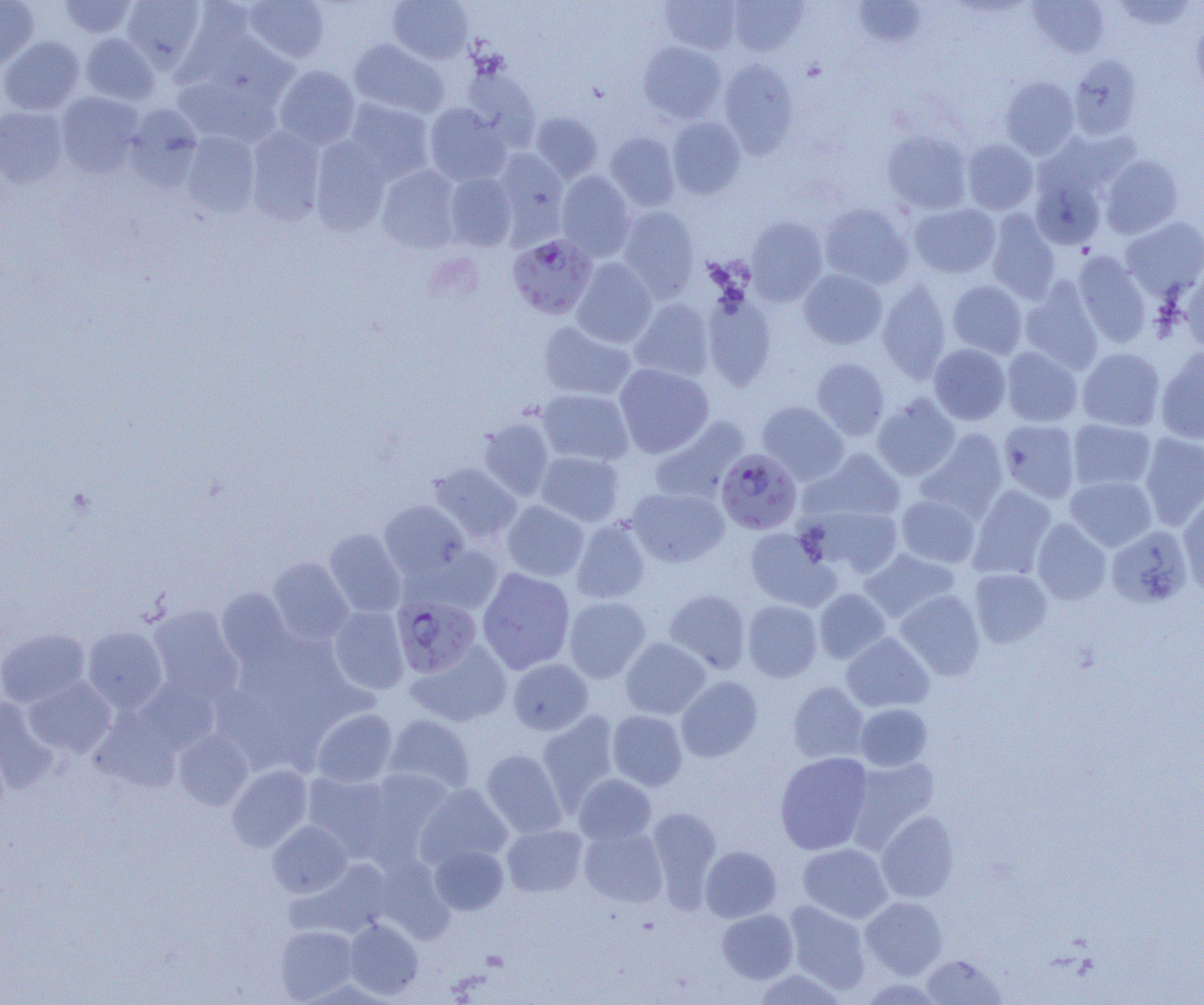 Approximate bounding boxes as (x1, y1, x2, y2) in pixels. Plasmodium falciparum-infected red blood cell locations: (507, 233, 597, 319), (716, 448, 801, 534), (392, 595, 482, 678). Uninfected red blood cell locations: (0, 0, 39, 70), (57, 0, 138, 39), (121, 0, 206, 71), (243, 0, 330, 63), (387, 0, 474, 64), (660, 0, 741, 54), (729, 0, 807, 56), (852, 0, 926, 48), (1027, 1, 1110, 59), (1109, 1, 1199, 31), (161, 3, 254, 89), (1192, 16, 1204, 100), (80, 33, 160, 105), (0, 36, 85, 115), (349, 38, 449, 118), (639, 41, 725, 123), (1069, 55, 1143, 140), (719, 59, 798, 156), (273, 65, 361, 149), (462, 67, 540, 148), (1000, 76, 1079, 158), (171, 84, 285, 146), (55, 92, 144, 176), (343, 98, 435, 184), (424, 103, 512, 186), (124, 104, 204, 189), (0, 106, 68, 188), (530, 111, 603, 183), (667, 117, 746, 198), (246, 127, 326, 224), (882, 130, 973, 215), (180, 132, 260, 217), (604, 132, 681, 211), (309, 137, 391, 235), (962, 139, 1038, 215), (492, 149, 569, 239), (1100, 154, 1184, 238), (377, 165, 463, 252), (556, 171, 635, 261), (444, 172, 517, 251), (1030, 173, 1106, 251), (819, 203, 914, 289), (908, 203, 1000, 278), (617, 206, 700, 301), (986, 210, 1061, 303), (745, 216, 828, 306), (1120, 216, 1204, 299), (1073, 252, 1152, 346), (571, 258, 658, 348), (1180, 268, 1204, 352), (798, 269, 887, 349), (877, 279, 951, 381), (947, 280, 1027, 358), (1020, 280, 1104, 373), (702, 294, 776, 390), (629, 298, 714, 382), (538, 321, 636, 401), (929, 344, 1011, 425), (1001, 346, 1083, 427), (1156, 346, 1204, 445), (1077, 347, 1165, 432), (811, 358, 890, 440), (614, 363, 713, 457), (537, 389, 634, 466), (872, 394, 960, 481), (758, 400, 848, 484), (476, 416, 555, 501), (648, 416, 749, 505), (998, 419, 1081, 503), (1068, 419, 1156, 492), (917, 429, 1009, 522), (1138, 432, 1204, 530), (805, 448, 907, 524), (535, 451, 625, 527), (427, 462, 522, 543), (1065, 475, 1157, 551), (968, 485, 1056, 580), (626, 487, 729, 567), (1178, 492, 1204, 596), (896, 494, 980, 567), (378, 500, 470, 581), (501, 501, 589, 581), (803, 503, 903, 578), (571, 518, 651, 604), (1032, 518, 1112, 605), (1105, 525, 1192, 608), (745, 527, 838, 611), (324, 529, 406, 617), (411, 544, 505, 615), (859, 548, 960, 623), (267, 557, 354, 644), (477, 568, 575, 675), (969, 569, 1052, 648), (216, 588, 293, 667), (813, 588, 891, 665), (665, 589, 751, 673), (895, 590, 985, 680), (564, 596, 651, 683), (742, 600, 822, 682), (148, 606, 243, 703), (329, 606, 410, 694), (82, 626, 167, 713), (0, 628, 89, 707), (841, 632, 934, 712), (620, 637, 711, 719), (406, 641, 511, 727), (508, 658, 593, 735), (676, 676, 763, 762), (24, 677, 116, 757), (134, 680, 219, 755), (787, 682, 869, 764), (0, 697, 56, 792), (855, 703, 932, 771), (90, 707, 182, 792), (311, 709, 398, 788), (607, 710, 688, 791), (537, 711, 621, 810), (384, 714, 476, 795), (173, 730, 253, 810), (481, 750, 567, 837), (775, 752, 873, 855), (845, 756, 939, 851), (227, 765, 313, 852), (360, 768, 457, 864), (302, 771, 398, 860), (574, 773, 656, 845), (414, 782, 512, 870), (646, 807, 722, 909), (876, 811, 959, 903), (267, 820, 352, 898), (502, 824, 588, 897), (578, 825, 667, 907), (798, 842, 892, 923), (429, 844, 508, 915), (699, 846, 781, 922), (372, 857, 454, 943), (860, 896, 947, 979), (784, 900, 871, 993), (717, 909, 798, 983), (344, 917, 423, 999), (275, 925, 359, 1003), (921, 954, 1005, 1004), (751, 969, 847, 1004). Slide-level diagnosis: Plasmodium falciparum. Image is 1204×1005 pixels. Thin blood film. Single field of view. 1000x magnification. Optical microscopy.